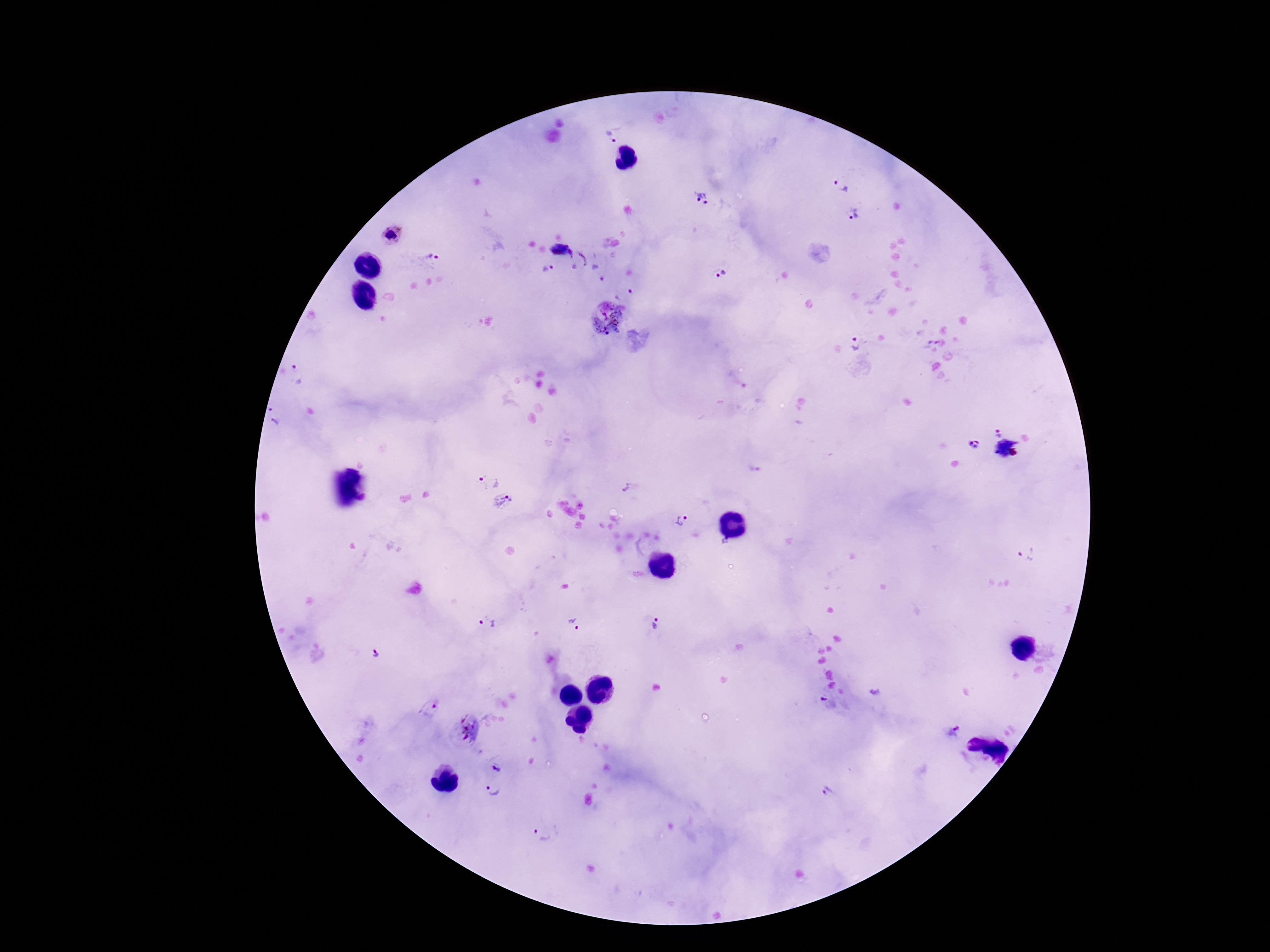 Approximate centers as (x, y) in pixels. Plasmodium parasite locations: (609, 136), (841, 185), (702, 197), (855, 213), (391, 235), (562, 251), (436, 257), (583, 258), (548, 268), (719, 275), (602, 280), (631, 292), (606, 316), (856, 343), (297, 374), (276, 416), (998, 433), (974, 445), (1006, 447), (1013, 452), (489, 479), (627, 487), (505, 502), (680, 521), (1027, 554), (575, 623), (487, 624), (655, 624), (379, 656), (429, 707), (467, 727), (955, 732), (496, 767), (492, 789), (830, 792), (543, 833). 100x magnification. Giemsa stain. Patient malaria status: infected. Image is 1270×952 pixels. Photographed through the microscope eyepiece with a smartphone camera. One field from this slide. Thick peripheral-blood smear.